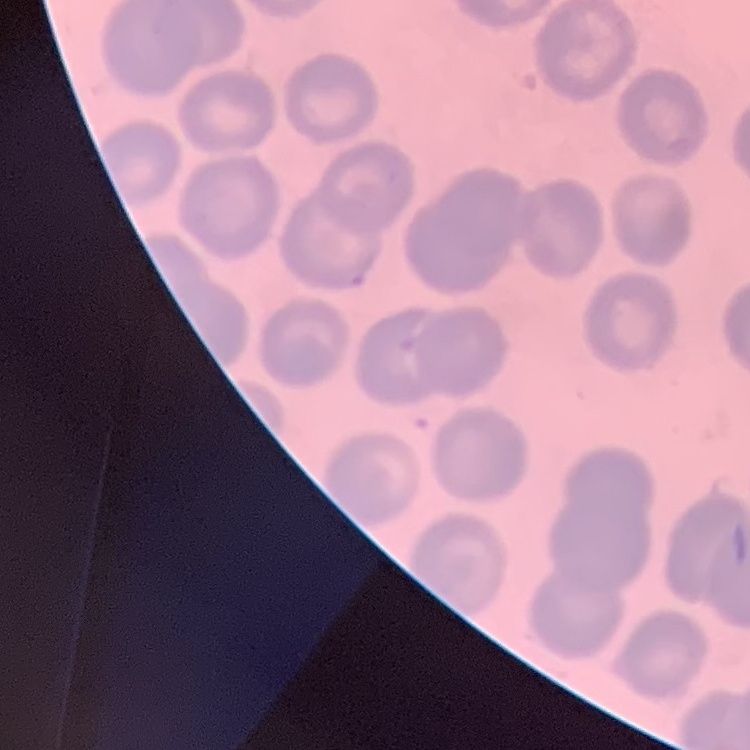

red blood cell morphology = no rouleaux formation
image type = square crop of a larger photomicrograph
preparation = thin peripheral smear
stain = Field's or Giemsa